Name the parasite shown.
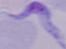
A trypanosome.

magnification = 1000x
modality = photomicrograph